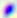

Summary:
  - Magnification: 400x
  - Identification: Toxoplasma gondii
  - Modality: micrograph